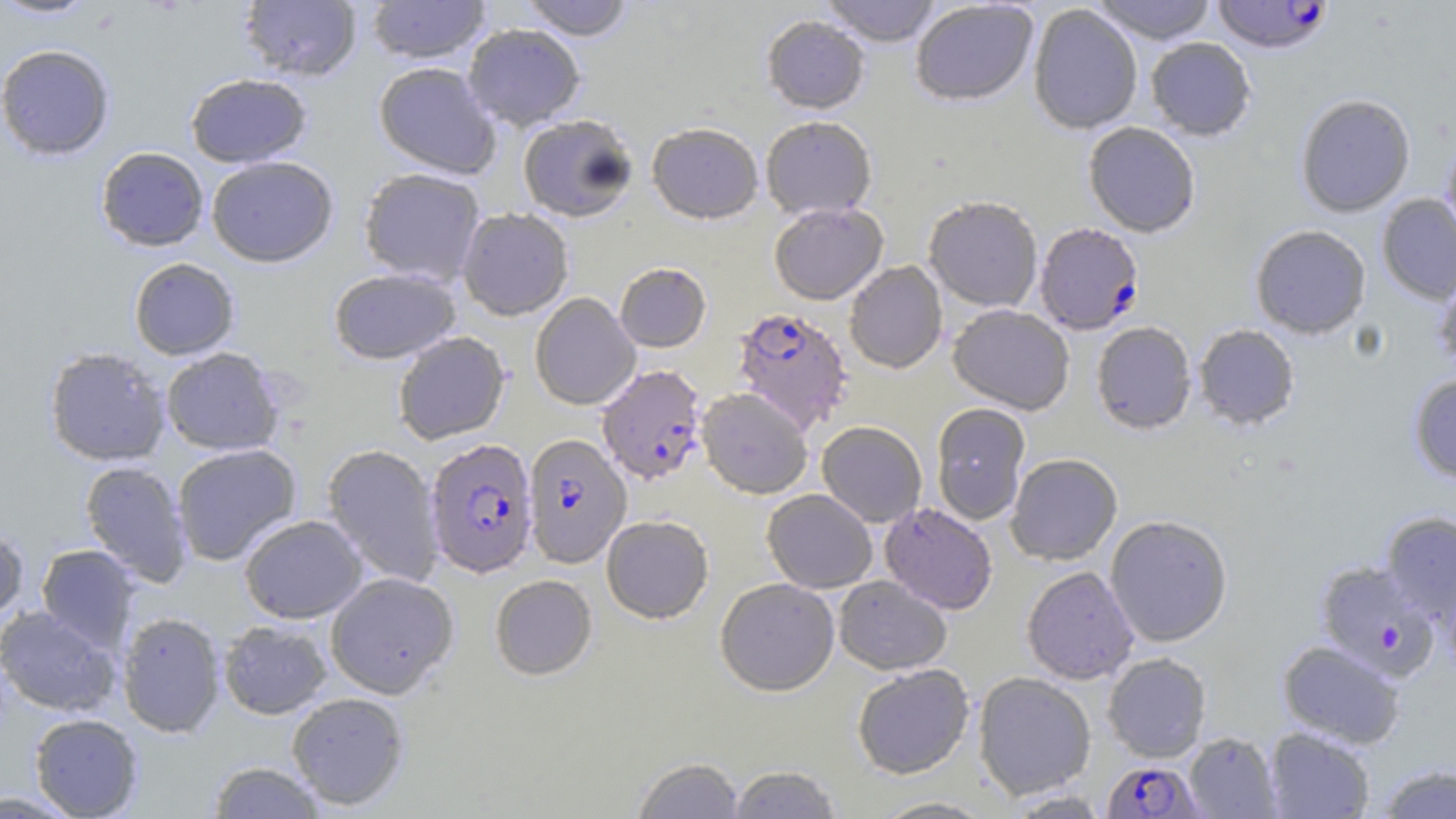

{
  "slide_level_diagnosis": "Plasmodium falciparum",
  "image_size": "1456×819 pixels",
  "stain": "May-Grünwald-Giemsa",
  "field_of_view": "one of a larger specimen",
  "preparation": "thin blood film",
  "modality": "optical microscopy",
  "plasmodium_falciparum_infected_red_blood_cell_locations": "approximate bounding boxes as named x1/y1/x2/y2 corners in pixels: (x1=1210, y1=0, x2=1335, y2=55), (x1=1034, y1=222, x2=1144, y2=335), (x1=732, y1=306, x2=852, y2=433), (x1=597, y1=364, x2=708, y2=484), (x1=522, y1=433, x2=631, y2=568), (x1=424, y1=437, x2=538, y2=578), (x1=1314, y1=559, x2=1441, y2=682), (x1=1102, y1=760, x2=1203, y2=818)",
  "uninfected_red_blood_cell_locations": "approximate bounding boxes as named x1/y1/x2/y2 corners in pixels: (x1=0, y1=0, x2=103, y2=20), (x1=238, y1=0, x2=363, y2=81), (x1=366, y1=0, x2=492, y2=64), (x1=519, y1=0, x2=636, y2=41), (x1=820, y1=0, x2=943, y2=46), (x1=910, y1=0, x2=1039, y2=106), (x1=1090, y1=0, x2=1217, y2=44), (x1=1028, y1=4, x2=1143, y2=134), (x1=761, y1=14, x2=870, y2=114), (x1=462, y1=23, x2=586, y2=131), (x1=1145, y1=37, x2=1257, y2=141), (x1=0, y1=44, x2=116, y2=161), (x1=373, y1=62, x2=501, y2=179), (x1=185, y1=73, x2=312, y2=168), (x1=1295, y1=93, x2=1416, y2=217), (x1=517, y1=114, x2=638, y2=222), (x1=760, y1=115, x2=877, y2=220), (x1=1083, y1=121, x2=1201, y2=237), (x1=647, y1=122, x2=764, y2=224), (x1=1441, y1=132, x2=1456, y2=250), (x1=95, y1=146, x2=209, y2=251), (x1=206, y1=156, x2=339, y2=267), (x1=358, y1=167, x2=486, y2=286), (x1=1376, y1=194, x2=1456, y2=304), (x1=923, y1=195, x2=1043, y2=312), (x1=769, y1=202, x2=888, y2=304), (x1=457, y1=207, x2=574, y2=321), (x1=1250, y1=225, x2=1371, y2=338), (x1=129, y1=258, x2=240, y2=360), (x1=844, y1=261, x2=947, y2=373), (x1=615, y1=262, x2=711, y2=352), (x1=329, y1=267, x2=461, y2=364), (x1=1432, y1=269, x2=1456, y2=375), (x1=530, y1=292, x2=641, y2=410), (x1=948, y1=304, x2=1075, y2=414), (x1=1091, y1=322, x2=1197, y2=434), (x1=1193, y1=324, x2=1300, y2=430), (x1=392, y1=331, x2=510, y2=445), (x1=43, y1=346, x2=171, y2=467), (x1=161, y1=348, x2=284, y2=456), (x1=1408, y1=374, x2=1456, y2=483), (x1=697, y1=387, x2=813, y2=499), (x1=931, y1=403, x2=1032, y2=524), (x1=817, y1=421, x2=927, y2=527), (x1=171, y1=443, x2=302, y2=566), (x1=322, y1=444, x2=444, y2=588), (x1=1005, y1=453, x2=1122, y2=565), (x1=79, y1=460, x2=193, y2=587), (x1=762, y1=489, x2=877, y2=593), (x1=879, y1=502, x2=998, y2=614), (x1=1380, y1=511, x2=1456, y2=622), (x1=239, y1=514, x2=368, y2=624), (x1=601, y1=514, x2=714, y2=624), (x1=1104, y1=514, x2=1233, y2=647), (x1=0, y1=522, x2=29, y2=625), (x1=37, y1=544, x2=140, y2=652), (x1=1022, y1=566, x2=1139, y2=685), (x1=325, y1=571, x2=459, y2=699), (x1=490, y1=574, x2=598, y2=680), (x1=834, y1=576, x2=952, y2=675), (x1=715, y1=577, x2=839, y2=696), (x1=0, y1=605, x2=121, y2=717), (x1=117, y1=611, x2=226, y2=738), (x1=218, y1=620, x2=333, y2=719), (x1=1277, y1=639, x2=1406, y2=748), (x1=1102, y1=653, x2=1212, y2=762), (x1=852, y1=664, x2=974, y2=779), (x1=973, y1=672, x2=1096, y2=799), (x1=287, y1=692, x2=410, y2=810), (x1=29, y1=713, x2=143, y2=818), (x1=1264, y1=727, x2=1375, y2=818), (x1=1183, y1=731, x2=1281, y2=818), (x1=632, y1=756, x2=745, y2=819), (x1=206, y1=760, x2=329, y2=818), (x1=1375, y1=763, x2=1456, y2=819), (x1=728, y1=764, x2=843, y2=818), (x1=0, y1=790, x2=84, y2=816), (x1=869, y1=796, x2=1000, y2=818)",
  "magnification": "1000x"
}